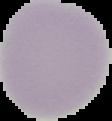
Summary:
  - Image type: cell region segmented out of the field of view; surrounding area masked to black
  - Image size: 112×121 pixels
  - Preparation: thin blood smear
  - Result: no Plasmodium parasites detected